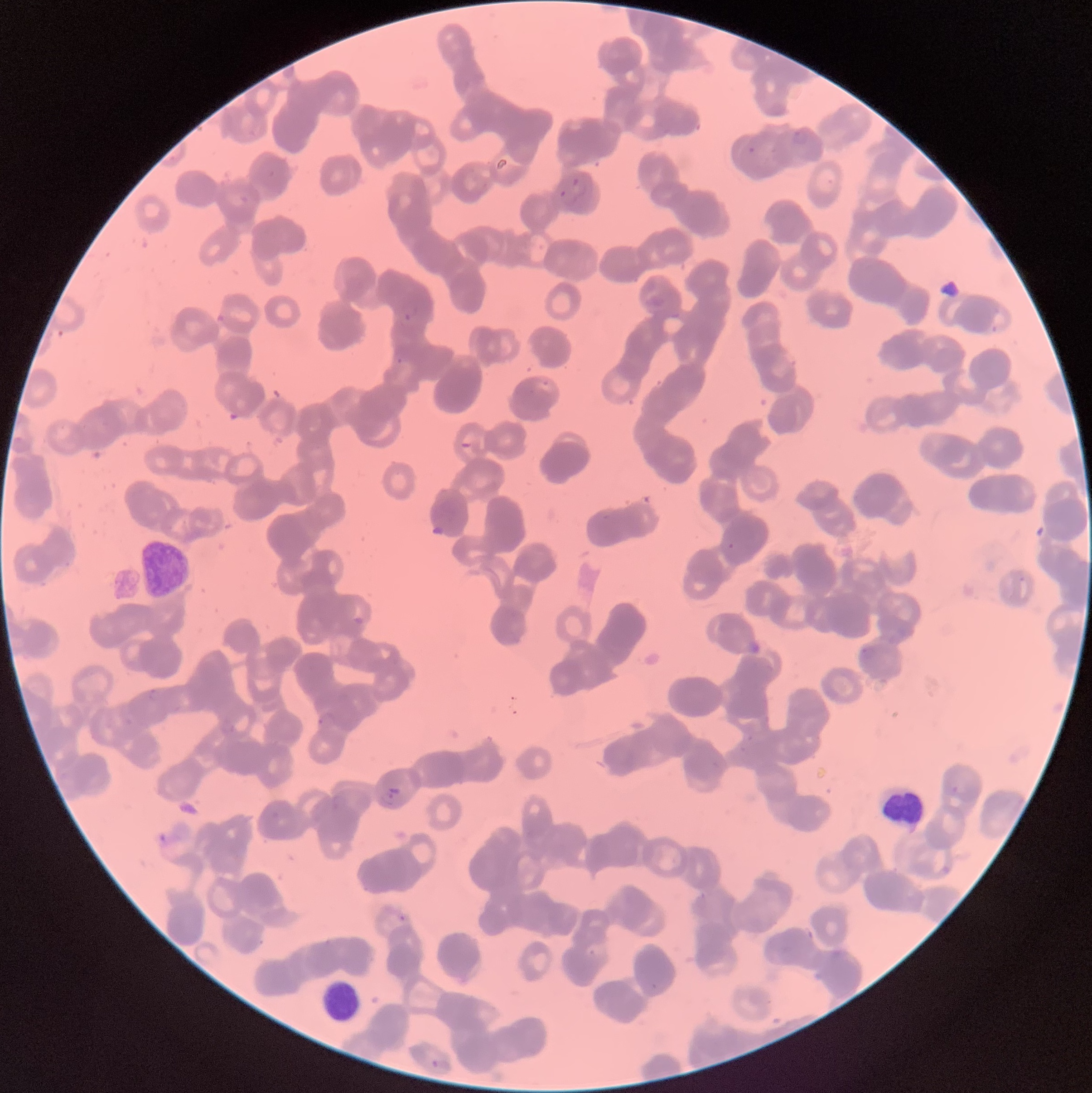

Approximate bounding boxes as (x1, y1, x2, y2) in pixels. Plasmodium parasites too small for a box (approximate centers as (x, y) in pixels): (400, 360), (730, 546). Plasmodium parasite locations: (747, 145, 756, 154), (571, 177, 581, 187), (557, 189, 567, 198), (403, 307, 418, 321), (535, 378, 552, 393), (460, 441, 475, 454), (860, 647, 875, 659), (149, 687, 162, 702), (317, 718, 324, 726), (384, 787, 399, 805), (399, 914, 406, 922), (431, 1057, 453, 1072). White blood cell locations: (137, 540, 193, 599), (879, 786, 924, 831), (320, 979, 361, 1021). Image is 1092×1093 pixels. Optical microscopy. The red blood cells show rouleaux formation. Thin blood film.